Identify the parasite.
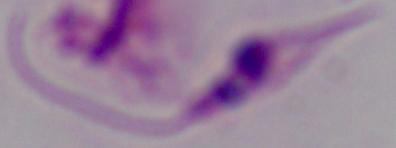
This is Leishmania.

Micrograph. 1000x magnification.